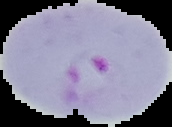

preparation = thin blood film
image type = segmented cell region with the area outside set to black
image size = 172×127 pixels
result = malaria parasites identified